Locate every blood parasite and identify its species.
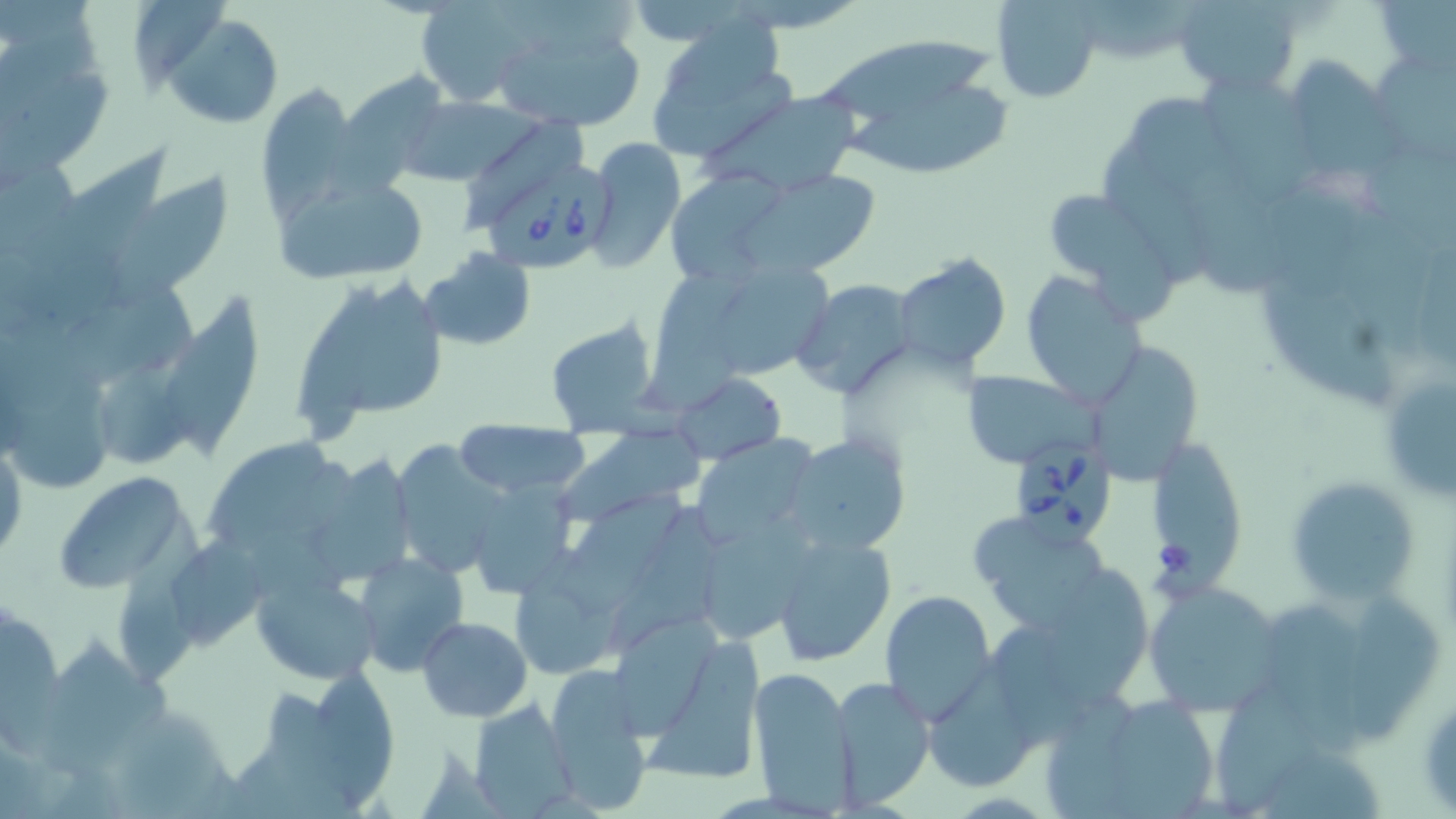
Approximate bounding boxes as named x1/y1/x2/y2 corners in pixels.
Babesia divergens-infected red blood cells: (x1=484, y1=163, x2=617, y2=274), (x1=1015, y1=431, x2=1117, y2=547).
No Plasmodium falciparum, Plasmodium ovale, Plasmodium malariae, Plasmodium vivax, or Trypanosoma brucei observed.

{
  "slide_level_diagnosis": "Babesia divergens",
  "image_size": "1456×819 pixels",
  "platelet_locations": "approximate bounding boxes as named x1/y1/x2/y2 corners in pixels: (x1=1155, y1=537, x2=1196, y2=580)",
  "stain": "May-Grünwald-Giemsa",
  "uninfected_red_blood_cell_locations": "approximate bounding boxes as named x1/y1/x2/y2 corners in pixels: (x1=507, y1=0, x2=640, y2=62), (x1=990, y1=0, x2=1102, y2=104), (x1=1173, y1=0, x2=1301, y2=94), (x1=1375, y1=0, x2=1456, y2=85), (x1=414, y1=2, x2=547, y2=107), (x1=1083, y1=4, x2=1201, y2=61), (x1=667, y1=7, x2=784, y2=91), (x1=164, y1=14, x2=283, y2=128), (x1=485, y1=17, x2=652, y2=130), (x1=0, y1=21, x2=114, y2=174), (x1=643, y1=32, x2=796, y2=165), (x1=818, y1=37, x2=994, y2=121), (x1=1378, y1=51, x2=1456, y2=161), (x1=1300, y1=60, x2=1405, y2=170), (x1=1204, y1=72, x2=1319, y2=194), (x1=340, y1=73, x2=448, y2=185), (x1=255, y1=82, x2=360, y2=222), (x1=707, y1=90, x2=861, y2=195), (x1=847, y1=90, x2=1013, y2=177), (x1=1141, y1=95, x2=1273, y2=296), (x1=399, y1=96, x2=525, y2=186), (x1=463, y1=119, x2=582, y2=229), (x1=582, y1=139, x2=686, y2=273), (x1=34, y1=141, x2=185, y2=268), (x1=1112, y1=146, x2=1215, y2=290), (x1=1367, y1=146, x2=1455, y2=245), (x1=734, y1=167, x2=883, y2=278), (x1=276, y1=172, x2=433, y2=288), (x1=671, y1=172, x2=781, y2=274), (x1=108, y1=173, x2=230, y2=308), (x1=1200, y1=181, x2=1357, y2=290), (x1=1046, y1=185, x2=1175, y2=323), (x1=1328, y1=197, x2=1427, y2=371), (x1=420, y1=247, x2=536, y2=350), (x1=897, y1=253, x2=1011, y2=372), (x1=721, y1=262, x2=830, y2=373), (x1=339, y1=271, x2=452, y2=419), (x1=1022, y1=271, x2=1146, y2=409), (x1=1263, y1=275, x2=1392, y2=409), (x1=290, y1=279, x2=392, y2=444), (x1=792, y1=279, x2=918, y2=399), (x1=71, y1=284, x2=201, y2=379), (x1=162, y1=292, x2=261, y2=459), (x1=545, y1=319, x2=663, y2=434), (x1=1087, y1=335, x2=1212, y2=492), (x1=1376, y1=355, x2=1455, y2=510), (x1=103, y1=362, x2=193, y2=463), (x1=13, y1=371, x2=115, y2=485), (x1=963, y1=371, x2=1098, y2=468), (x1=673, y1=372, x2=785, y2=463), (x1=560, y1=419, x2=712, y2=529), (x1=455, y1=422, x2=589, y2=498), (x1=783, y1=430, x2=912, y2=555), (x1=690, y1=436, x2=815, y2=547), (x1=391, y1=438, x2=506, y2=579), (x1=203, y1=439, x2=329, y2=542), (x1=1154, y1=441, x2=1241, y2=589), (x1=0, y1=442, x2=26, y2=564), (x1=312, y1=452, x2=420, y2=579), (x1=462, y1=470, x2=586, y2=598), (x1=50, y1=471, x2=197, y2=593), (x1=1286, y1=475, x2=1420, y2=602), (x1=562, y1=484, x2=693, y2=622), (x1=113, y1=505, x2=205, y2=687), (x1=607, y1=507, x2=724, y2=651), (x1=704, y1=512, x2=818, y2=643), (x1=971, y1=514, x2=1113, y2=634), (x1=770, y1=532, x2=895, y2=666), (x1=173, y1=540, x2=270, y2=650), (x1=353, y1=552, x2=469, y2=676), (x1=1048, y1=563, x2=1149, y2=706), (x1=252, y1=572, x2=382, y2=686), (x1=1142, y1=580, x2=1286, y2=713), (x1=879, y1=589, x2=996, y2=723), (x1=1349, y1=592, x2=1440, y2=745), (x1=1263, y1=599, x2=1371, y2=752), (x1=0, y1=610, x2=60, y2=764), (x1=617, y1=615, x2=725, y2=735), (x1=416, y1=616, x2=533, y2=721), (x1=41, y1=631, x2=164, y2=767), (x1=641, y1=633, x2=766, y2=784), (x1=312, y1=662, x2=399, y2=810), (x1=745, y1=665, x2=856, y2=810), (x1=930, y1=668, x2=1031, y2=789), (x1=544, y1=669, x2=654, y2=814), (x1=832, y1=676, x2=934, y2=807), (x1=271, y1=683, x2=357, y2=810), (x1=1041, y1=686, x2=1134, y2=819), (x1=1218, y1=686, x2=1325, y2=817), (x1=116, y1=698, x2=228, y2=819), (x1=1113, y1=698, x2=1216, y2=819), (x1=469, y1=699, x2=577, y2=817)",
  "preparation": "thin blood smear",
  "field_of_view": "single",
  "magnification": "1000x",
  "modality": "light microscopy"
}